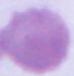 1000x magnification. A red blood cell is seen. Micrograph.